Assess the morphology of the erythrocytes.
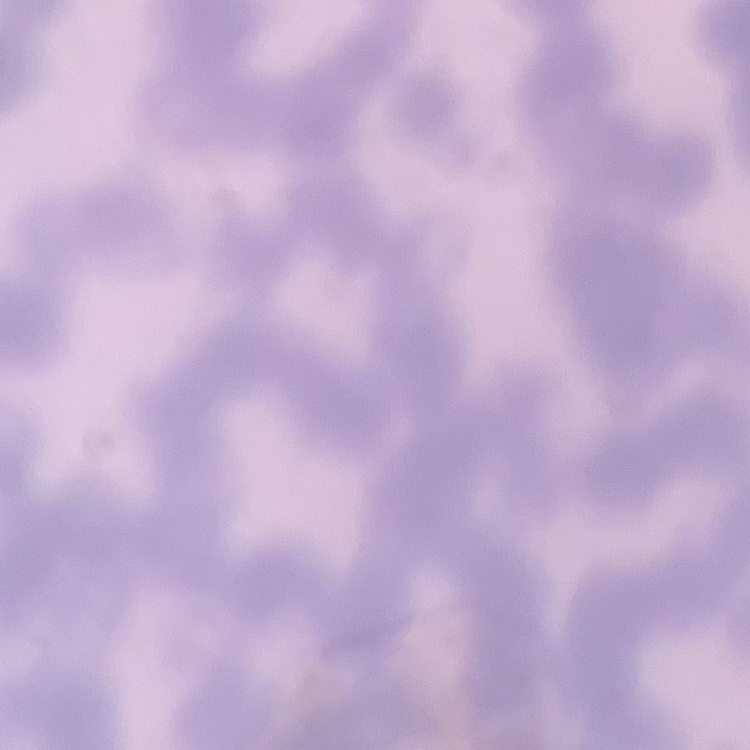

Rouleaux formation.

Stained with either Field's or Giemsa. One tile cut from a larger photomicrograph. Thin blood smear.